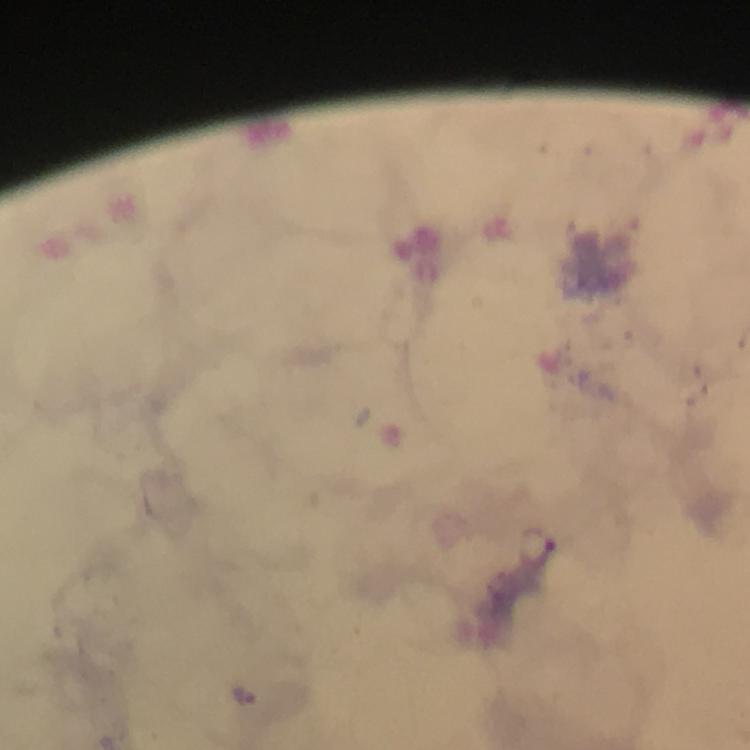
{
  "cropped_from": "a single field of view",
  "immersion_oil": "applied",
  "plasmodium_parasite_locations": "approximate centers as (x, y) in pixels: (247, 695)",
  "image_size": "750×750 pixels",
  "preparation": "thick smear",
  "capture": "smartphone mounted on the microscope",
  "magnification": "100x",
  "context": "from a diagnostic examination for malaria",
  "stain": "Giemsa"
}